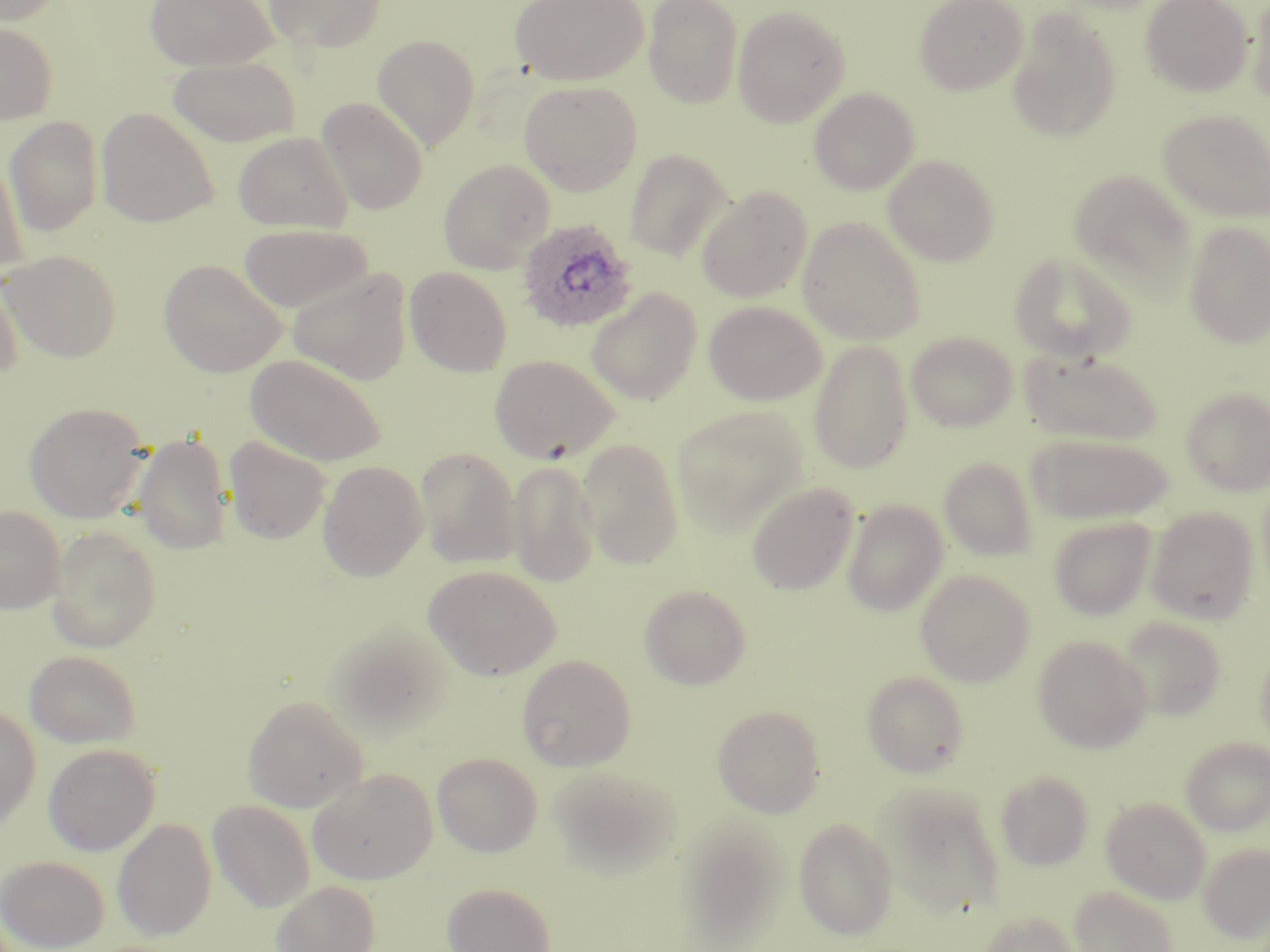

Plasmodium ovale-infected red blood cell locations = approximate bounding boxes as (x1,y1)-(x2,y2) corner pairs in pixels: (517,218)-(638,334)
slide-level diagnosis = Plasmodium ovale
field of view = single
stain = May-Grünwald-Giemsa
uninfected red blood cell locations = approximate bounding boxes as (x1,y1)-(x2,y2) corner pairs in pixels: (0,0)-(66,26), (144,0)-(278,71), (264,0)-(386,52), (509,0)-(647,85), (643,0)-(744,108), (914,0)-(1028,95), (1141,0)-(1252,96), (1244,0)-(1270,107), (731,5)-(851,128), (1007,7)-(1121,143), (0,21)-(57,125), (371,34)-(480,151), (167,55)-(301,147), (520,81)-(642,195), (809,87)-(919,195), (316,97)-(428,215), (95,107)-(219,228), (1158,110)-(1270,223), (3,115)-(104,236), (233,131)-(353,233), (1,149)-(30,280), (624,149)-(731,260), (882,154)-(1000,266), (437,158)-(556,274), (1069,171)-(1198,304), (696,186)-(813,303), (797,216)-(925,345), (1182,221)-(1269,349), (238,222)-(373,313), (2,248)-(122,362), (1009,250)-(1137,364), (158,258)-(287,377), (404,266)-(512,376), (287,267)-(413,385), (0,268)-(24,382), (585,287)-(703,405), (703,300)-(825,405), (906,331)-(1017,432), (809,340)-(913,474), (1020,348)-(1163,445), (245,354)-(387,466), (489,354)-(620,464), (1180,386)-(1270,495), (23,401)-(150,523), (672,405)-(810,536), (132,432)-(233,554), (1026,434)-(1173,524), (224,437)-(331,544), (576,438)-(684,569), (415,446)-(522,568), (938,457)-(1038,562), (506,459)-(601,587), (318,460)-(428,582), (747,481)-(859,595), (842,499)-(948,616), (0,505)-(66,614), (1146,507)-(1259,624), (1049,517)-(1156,620), (47,526)-(163,652), (423,565)-(562,681), (915,569)-(1035,686), (639,584)-(751,690), (1117,616)-(1227,721), (324,619)-(455,738), (1032,634)-(1152,753), (1255,644)-(1270,754), (25,649)-(142,749), (516,654)-(636,771), (862,671)-(968,778), (242,694)-(368,812), (0,704)-(41,830), (712,704)-(826,817), (1181,737)-(1270,835), (43,743)-(160,856), (432,752)-(542,856), (547,764)-(683,877), (308,768)-(437,885), (995,769)-(1094,870), (875,781)-(1006,918), (1101,797)-(1210,904), (208,799)-(315,913), (112,817)-(216,941), (794,818)-(898,940), (1199,842)-(1270,943), (1,855)-(109,952), (271,880)-(380,952), (441,882)-(556,952), (1069,885)-(1177,952), (975,911)-(1081,952)
image size = 1270×952 pixels
modality = optical microscopy
preparation = thin blood smear
magnification = 1000x